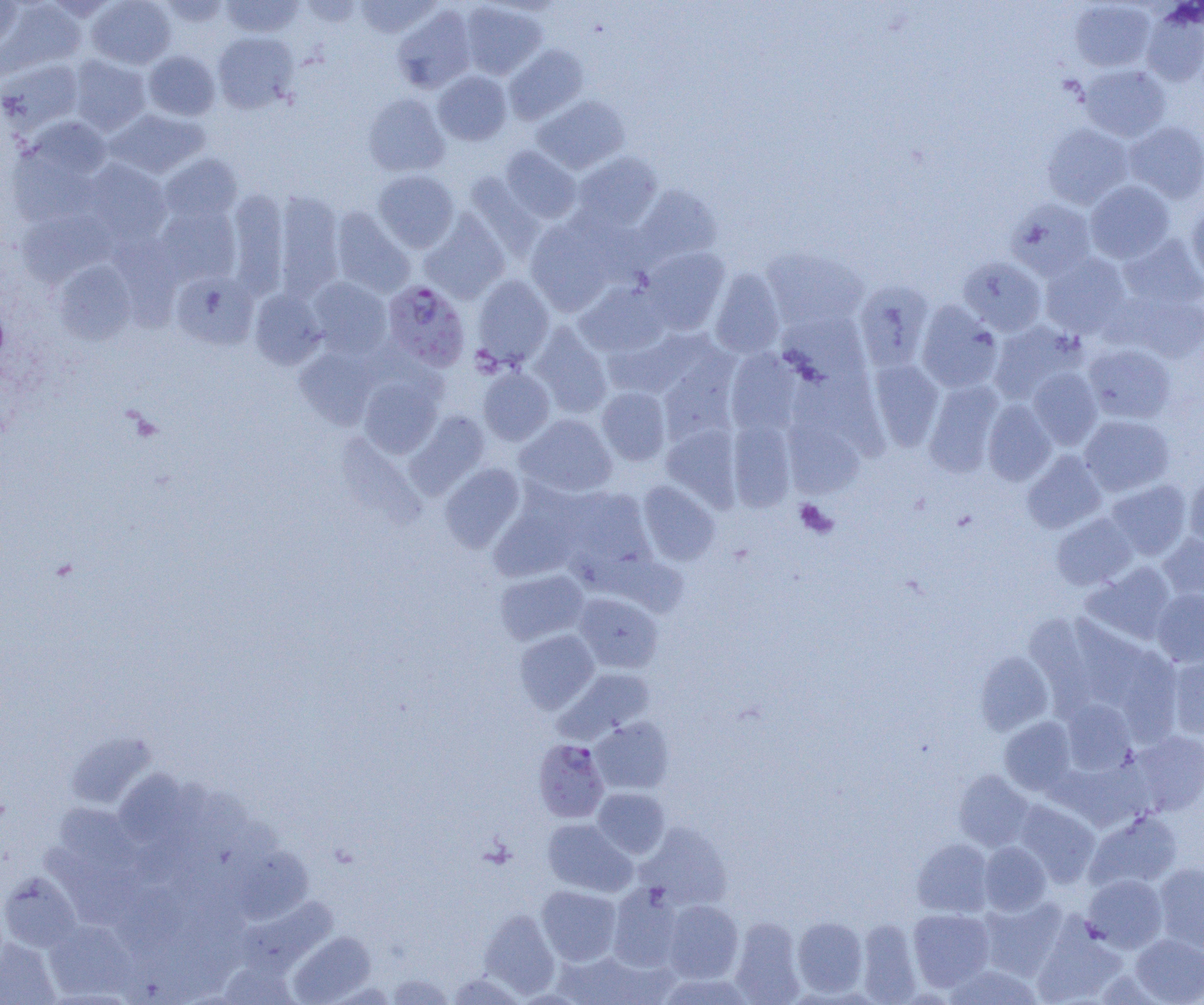
slide-level diagnosis = Plasmodium falciparum
magnification = 1000x
image size = 1204×1005 pixels
preparation = thin blood film
field of view = one of a larger specimen
modality = optical microscopy
Plasmodium falciparum-infected red blood cell locations = approximate bounding boxes as named x1/y1/x2/y2 corners in pixels: (x1=382, y1=280, x2=471, y2=371), (x1=533, y1=739, x2=609, y2=822)
platelet locations = approximate bounding boxes as named x1/y1/x2/y2 corners in pixels: (x1=794, y1=499, x2=837, y2=538)
uninfected red blood cell locations = approximate bounding boxes as named x1/y1/x2/y2 corners in pixels: (x1=87, y1=0, x2=176, y2=69), (x1=157, y1=0, x2=232, y2=27), (x1=221, y1=0, x2=303, y2=37), (x1=299, y1=0, x2=362, y2=26), (x1=355, y1=0, x2=441, y2=38), (x1=0, y1=1, x2=24, y2=52), (x1=2, y1=1, x2=86, y2=76), (x1=459, y1=1, x2=546, y2=79), (x1=1070, y1=1, x2=1155, y2=72), (x1=393, y1=5, x2=476, y2=93), (x1=1141, y1=5, x2=1204, y2=87), (x1=213, y1=32, x2=298, y2=114), (x1=504, y1=44, x2=588, y2=124), (x1=144, y1=51, x2=220, y2=121), (x1=69, y1=55, x2=151, y2=135), (x1=0, y1=58, x2=83, y2=134), (x1=1079, y1=64, x2=1171, y2=141), (x1=433, y1=71, x2=512, y2=145), (x1=363, y1=94, x2=450, y2=177), (x1=533, y1=95, x2=630, y2=173), (x1=105, y1=108, x2=209, y2=179), (x1=13, y1=116, x2=113, y2=199), (x1=1124, y1=121, x2=1204, y2=203), (x1=1042, y1=123, x2=1133, y2=209), (x1=500, y1=146, x2=581, y2=223), (x1=572, y1=152, x2=662, y2=232), (x1=159, y1=153, x2=242, y2=223), (x1=83, y1=159, x2=172, y2=244), (x1=373, y1=169, x2=459, y2=252), (x1=464, y1=173, x2=544, y2=260), (x1=1085, y1=180, x2=1176, y2=264), (x1=634, y1=185, x2=722, y2=265), (x1=225, y1=188, x2=289, y2=299), (x1=273, y1=192, x2=345, y2=299), (x1=1006, y1=198, x2=1096, y2=280), (x1=1186, y1=201, x2=1204, y2=285), (x1=155, y1=204, x2=240, y2=285), (x1=330, y1=207, x2=415, y2=298), (x1=18, y1=209, x2=117, y2=287), (x1=419, y1=211, x2=510, y2=303), (x1=526, y1=219, x2=615, y2=315), (x1=111, y1=234, x2=182, y2=329), (x1=1119, y1=234, x2=1203, y2=310), (x1=640, y1=246, x2=730, y2=334), (x1=762, y1=247, x2=868, y2=331), (x1=1040, y1=253, x2=1131, y2=338), (x1=958, y1=256, x2=1046, y2=335), (x1=53, y1=261, x2=136, y2=345), (x1=710, y1=269, x2=785, y2=359), (x1=171, y1=271, x2=257, y2=350), (x1=472, y1=275, x2=555, y2=368), (x1=307, y1=277, x2=392, y2=357), (x1=854, y1=280, x2=934, y2=371), (x1=576, y1=281, x2=669, y2=357), (x1=249, y1=288, x2=327, y2=369), (x1=1116, y1=292, x2=1204, y2=363), (x1=917, y1=301, x2=1002, y2=393), (x1=777, y1=313, x2=870, y2=387), (x1=989, y1=321, x2=1085, y2=404), (x1=528, y1=323, x2=613, y2=418), (x1=606, y1=329, x2=706, y2=399), (x1=1083, y1=344, x2=1175, y2=424), (x1=295, y1=345, x2=379, y2=429), (x1=726, y1=349, x2=801, y2=435), (x1=658, y1=356, x2=739, y2=447), (x1=867, y1=359, x2=944, y2=451), (x1=478, y1=366, x2=555, y2=445), (x1=1028, y1=368, x2=1103, y2=449), (x1=358, y1=375, x2=443, y2=458), (x1=924, y1=381, x2=1003, y2=477), (x1=597, y1=387, x2=671, y2=465), (x1=983, y1=400, x2=1056, y2=486), (x1=406, y1=410, x2=489, y2=499), (x1=516, y1=414, x2=617, y2=498), (x1=1079, y1=415, x2=1174, y2=496), (x1=783, y1=416, x2=864, y2=499), (x1=728, y1=419, x2=795, y2=512), (x1=662, y1=425, x2=742, y2=511), (x1=1022, y1=451, x2=1106, y2=534), (x1=440, y1=463, x2=525, y2=552), (x1=1183, y1=473, x2=1204, y2=552), (x1=1106, y1=480, x2=1192, y2=559), (x1=638, y1=481, x2=720, y2=566), (x1=560, y1=488, x2=655, y2=580), (x1=489, y1=498, x2=582, y2=582), (x1=1051, y1=513, x2=1137, y2=590), (x1=1158, y1=534, x2=1204, y2=604), (x1=1082, y1=562, x2=1176, y2=645), (x1=495, y1=569, x2=589, y2=645), (x1=1152, y1=589, x2=1204, y2=666), (x1=574, y1=592, x2=663, y2=672), (x1=1066, y1=616, x2=1146, y2=706), (x1=514, y1=630, x2=599, y2=713), (x1=1114, y1=649, x2=1184, y2=741), (x1=975, y1=651, x2=1053, y2=734), (x1=1167, y1=654, x2=1204, y2=739), (x1=555, y1=668, x2=656, y2=743), (x1=1060, y1=699, x2=1136, y2=774), (x1=590, y1=717, x2=673, y2=795), (x1=1000, y1=717, x2=1077, y2=795), (x1=1128, y1=730, x2=1204, y2=816), (x1=65, y1=731, x2=156, y2=810), (x1=1053, y1=759, x2=1151, y2=831), (x1=114, y1=770, x2=189, y2=847), (x1=953, y1=770, x2=1034, y2=851), (x1=592, y1=788, x2=670, y2=859), (x1=1015, y1=800, x2=1100, y2=887), (x1=52, y1=802, x2=145, y2=881), (x1=1086, y1=811, x2=1182, y2=891), (x1=542, y1=818, x2=637, y2=896), (x1=637, y1=824, x2=732, y2=910), (x1=912, y1=838, x2=994, y2=917), (x1=979, y1=842, x2=1051, y2=915), (x1=227, y1=845, x2=313, y2=924), (x1=1154, y1=863, x2=1204, y2=952), (x1=0, y1=871, x2=81, y2=952), (x1=1082, y1=874, x2=1168, y2=953), (x1=607, y1=884, x2=684, y2=971), (x1=537, y1=885, x2=621, y2=966), (x1=236, y1=897, x2=338, y2=977), (x1=979, y1=897, x2=1067, y2=980), (x1=662, y1=899, x2=743, y2=983), (x1=909, y1=908, x2=995, y2=991), (x1=479, y1=909, x2=560, y2=998), (x1=793, y1=916, x2=868, y2=996), (x1=729, y1=917, x2=805, y2=1004), (x1=856, y1=919, x2=921, y2=1004), (x1=45, y1=920, x2=136, y2=999), (x1=1032, y1=922, x2=1126, y2=1005), (x1=288, y1=931, x2=375, y2=1004), (x1=1131, y1=933, x2=1204, y2=1004), (x1=0, y1=939, x2=60, y2=1005), (x1=553, y1=950, x2=661, y2=1005), (x1=220, y1=960, x2=300, y2=1004), (x1=944, y1=962, x2=1044, y2=1004), (x1=448, y1=973, x2=527, y2=1005), (x1=386, y1=974, x2=455, y2=1004)